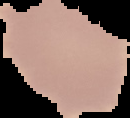
{
  "preparation": "thin blood film",
  "image_type": "segmented cell region on a black background",
  "image_size": "130×118 pixels",
  "malaria_status": "uninfected"
}